Identify the blood parasite species.
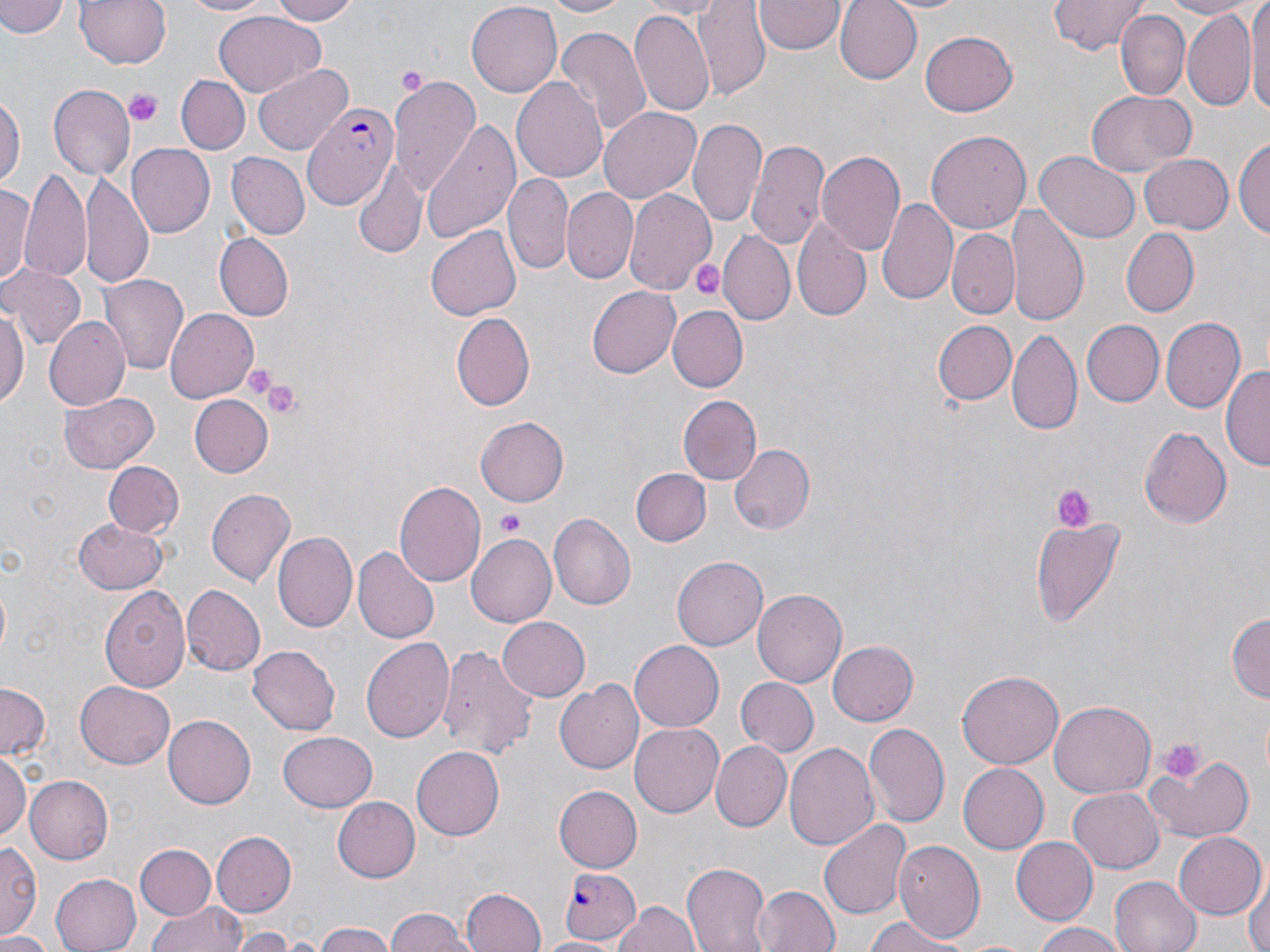
Plasmodium falciparum.

preparation = thin blood smear
image size = 1270×952 pixels
stain = May-Grünwald-Giemsa
modality = optical microscopy
Plasmodium falciparum-infected red blood cell locations = approximate bounding boxes as named x1/y1/x2/y2 corners in pixels: (x1=300, y1=101, x2=399, y2=212), (x1=556, y1=866, x2=640, y2=944)
uninfected red blood cell locations = approximate bounding boxes as named x1/y1/x2/y2 corners in pixels: (x1=0, y1=0, x2=69, y2=39), (x1=74, y1=0, x2=172, y2=70), (x1=177, y1=0, x2=277, y2=18), (x1=263, y1=0, x2=362, y2=25), (x1=543, y1=0, x2=637, y2=17), (x1=631, y1=0, x2=729, y2=19), (x1=695, y1=0, x2=770, y2=98), (x1=835, y1=0, x2=923, y2=84), (x1=1049, y1=0, x2=1147, y2=55), (x1=1153, y1=0, x2=1253, y2=16), (x1=1245, y1=0, x2=1270, y2=124), (x1=468, y1=1, x2=562, y2=94), (x1=754, y1=1, x2=844, y2=55), (x1=877, y1=1, x2=978, y2=15), (x1=696, y1=2, x2=837, y2=73), (x1=630, y1=8, x2=717, y2=118), (x1=1117, y1=10, x2=1188, y2=102), (x1=1182, y1=10, x2=1256, y2=112), (x1=215, y1=12, x2=325, y2=96), (x1=555, y1=26, x2=649, y2=137), (x1=918, y1=29, x2=1018, y2=116), (x1=254, y1=63, x2=353, y2=155), (x1=389, y1=73, x2=483, y2=197), (x1=176, y1=75, x2=248, y2=154), (x1=512, y1=78, x2=608, y2=183), (x1=47, y1=83, x2=135, y2=182), (x1=1087, y1=89, x2=1194, y2=175), (x1=0, y1=92, x2=23, y2=189), (x1=600, y1=108, x2=702, y2=203), (x1=421, y1=117, x2=521, y2=244), (x1=689, y1=118, x2=765, y2=227), (x1=925, y1=130, x2=1031, y2=235), (x1=1235, y1=133, x2=1270, y2=243), (x1=747, y1=138, x2=829, y2=253), (x1=127, y1=144, x2=214, y2=237), (x1=817, y1=148, x2=907, y2=257), (x1=1035, y1=151, x2=1138, y2=245), (x1=227, y1=152, x2=308, y2=239), (x1=1140, y1=154, x2=1232, y2=234), (x1=353, y1=159, x2=424, y2=260), (x1=20, y1=170, x2=93, y2=286), (x1=83, y1=170, x2=155, y2=291), (x1=504, y1=173, x2=572, y2=275), (x1=2, y1=180, x2=37, y2=289), (x1=624, y1=186, x2=715, y2=294), (x1=564, y1=188, x2=637, y2=283), (x1=875, y1=198, x2=957, y2=307), (x1=1007, y1=205, x2=1088, y2=324), (x1=793, y1=215, x2=872, y2=321), (x1=426, y1=227, x2=520, y2=320), (x1=1120, y1=227, x2=1200, y2=317), (x1=719, y1=229, x2=795, y2=326), (x1=947, y1=229, x2=1018, y2=318), (x1=217, y1=233, x2=294, y2=320), (x1=0, y1=265, x2=84, y2=351), (x1=101, y1=275, x2=188, y2=376), (x1=587, y1=287, x2=680, y2=377), (x1=0, y1=301, x2=29, y2=415), (x1=666, y1=306, x2=747, y2=392), (x1=165, y1=309, x2=259, y2=403), (x1=452, y1=313, x2=535, y2=408), (x1=43, y1=314, x2=130, y2=411), (x1=1160, y1=317, x2=1244, y2=413), (x1=932, y1=319, x2=1015, y2=403), (x1=1079, y1=320, x2=1163, y2=407), (x1=1006, y1=326, x2=1081, y2=439), (x1=1224, y1=363, x2=1270, y2=473), (x1=59, y1=391, x2=161, y2=474), (x1=187, y1=394, x2=272, y2=477), (x1=677, y1=394, x2=763, y2=488), (x1=475, y1=417, x2=569, y2=505), (x1=1139, y1=426, x2=1231, y2=530), (x1=727, y1=443, x2=813, y2=535), (x1=103, y1=462, x2=182, y2=537), (x1=631, y1=468, x2=711, y2=546), (x1=393, y1=481, x2=485, y2=590), (x1=205, y1=486, x2=295, y2=587), (x1=549, y1=512, x2=636, y2=611), (x1=1030, y1=514, x2=1126, y2=630), (x1=74, y1=516, x2=168, y2=591), (x1=273, y1=532, x2=357, y2=633), (x1=467, y1=533, x2=556, y2=627), (x1=353, y1=547, x2=439, y2=643), (x1=673, y1=556, x2=768, y2=650), (x1=100, y1=584, x2=190, y2=693), (x1=183, y1=584, x2=267, y2=675), (x1=752, y1=588, x2=847, y2=685), (x1=1228, y1=612, x2=1268, y2=707), (x1=497, y1=616, x2=591, y2=701), (x1=359, y1=637, x2=455, y2=744), (x1=629, y1=640, x2=724, y2=731), (x1=829, y1=641, x2=918, y2=725), (x1=248, y1=645, x2=340, y2=734), (x1=439, y1=646, x2=538, y2=761), (x1=956, y1=671, x2=1063, y2=769), (x1=736, y1=677, x2=816, y2=757), (x1=553, y1=679, x2=642, y2=776), (x1=74, y1=682, x2=175, y2=769), (x1=0, y1=683, x2=51, y2=761), (x1=1051, y1=700, x2=1155, y2=796), (x1=163, y1=715, x2=256, y2=808), (x1=864, y1=722, x2=949, y2=826), (x1=630, y1=724, x2=723, y2=815), (x1=277, y1=733, x2=376, y2=811), (x1=711, y1=741, x2=792, y2=833), (x1=784, y1=742, x2=879, y2=850), (x1=412, y1=746, x2=504, y2=841), (x1=0, y1=754, x2=29, y2=843), (x1=1146, y1=756, x2=1255, y2=844), (x1=959, y1=763, x2=1049, y2=854), (x1=24, y1=776, x2=113, y2=865), (x1=553, y1=786, x2=642, y2=870), (x1=1069, y1=788, x2=1164, y2=872), (x1=331, y1=796, x2=420, y2=883), (x1=817, y1=816, x2=912, y2=922), (x1=211, y1=832, x2=297, y2=916), (x1=1174, y1=833, x2=1264, y2=918), (x1=1010, y1=837, x2=1097, y2=926), (x1=896, y1=840, x2=986, y2=940), (x1=0, y1=842, x2=41, y2=940), (x1=135, y1=844, x2=217, y2=920), (x1=681, y1=863, x2=770, y2=952), (x1=51, y1=873, x2=140, y2=951), (x1=1247, y1=875, x2=1269, y2=952), (x1=1109, y1=876, x2=1200, y2=952), (x1=753, y1=884, x2=841, y2=952), (x1=460, y1=888, x2=545, y2=952), (x1=148, y1=899, x2=248, y2=952), (x1=612, y1=900, x2=700, y2=952), (x1=383, y1=910, x2=475, y2=952), (x1=861, y1=917, x2=965, y2=952), (x1=1032, y1=921, x2=1131, y2=952), (x1=313, y1=924, x2=398, y2=952), (x1=234, y1=927, x2=294, y2=952), (x1=0, y1=932, x2=55, y2=952), (x1=535, y1=935, x2=621, y2=952)
field of view = single
platelet locations = approximate bounding boxes as named x1/y1/x2/y2 corners in pixels: (x1=397, y1=66, x2=428, y2=97), (x1=126, y1=89, x2=164, y2=127), (x1=690, y1=260, x2=735, y2=304), (x1=239, y1=362, x2=286, y2=402), (x1=259, y1=377, x2=306, y2=418), (x1=1050, y1=485, x2=1093, y2=531), (x1=497, y1=513, x2=525, y2=536), (x1=1156, y1=735, x2=1204, y2=783)
magnification = 1000x